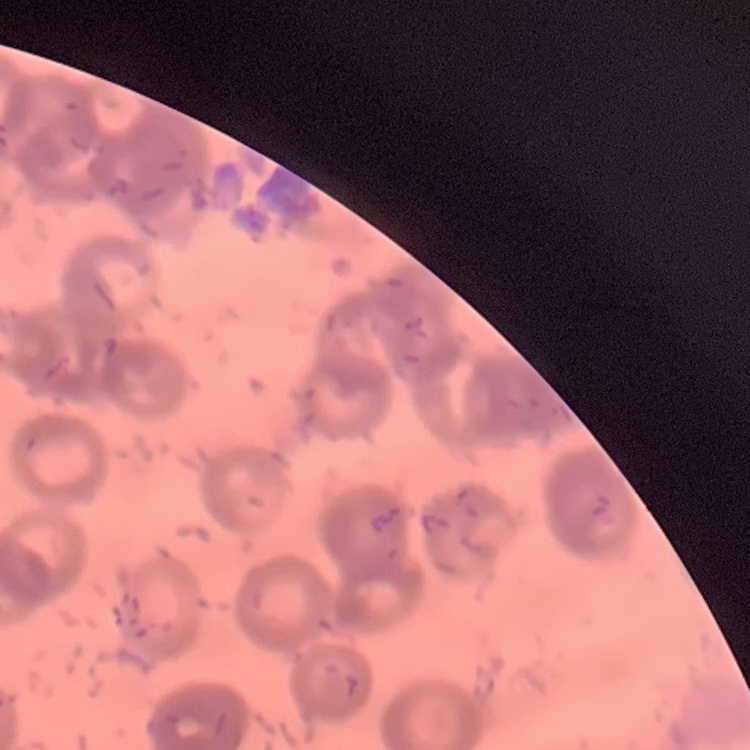

Summary:
  - Red blood cell morphology: rouleaux formation
  - Image type: one tile cut from a larger photomicrograph
  - Preparation: thin blood smear
  - Stain: Field's or Giemsa